State the preparation type.
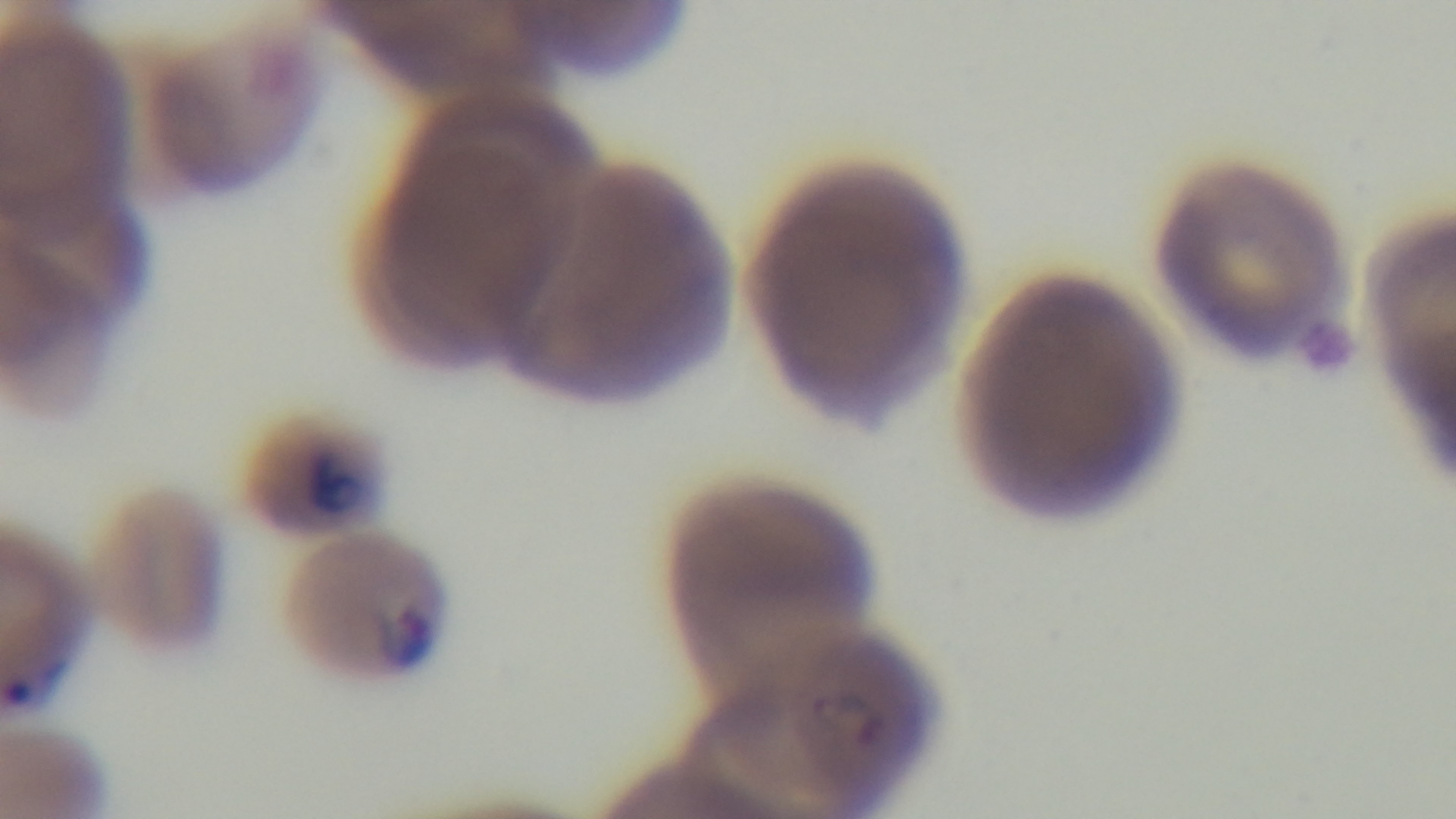

A thin smear.

Mounted 4K digital camera. Oil-immersion objective, 100x. One field from the slide. Light microscopy. Giemsa stain. Malaria status: positive.